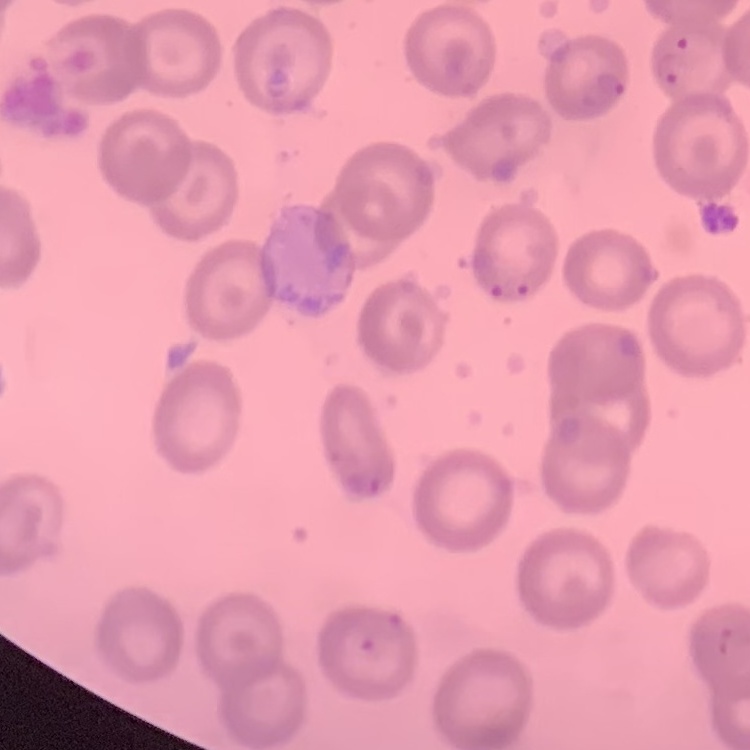

red blood cell morphology = no rouleaux formation
stain = Field's or Giemsa
image type = one tile cut from a larger photomicrograph
preparation = thin blood smear